Give the preparation type.
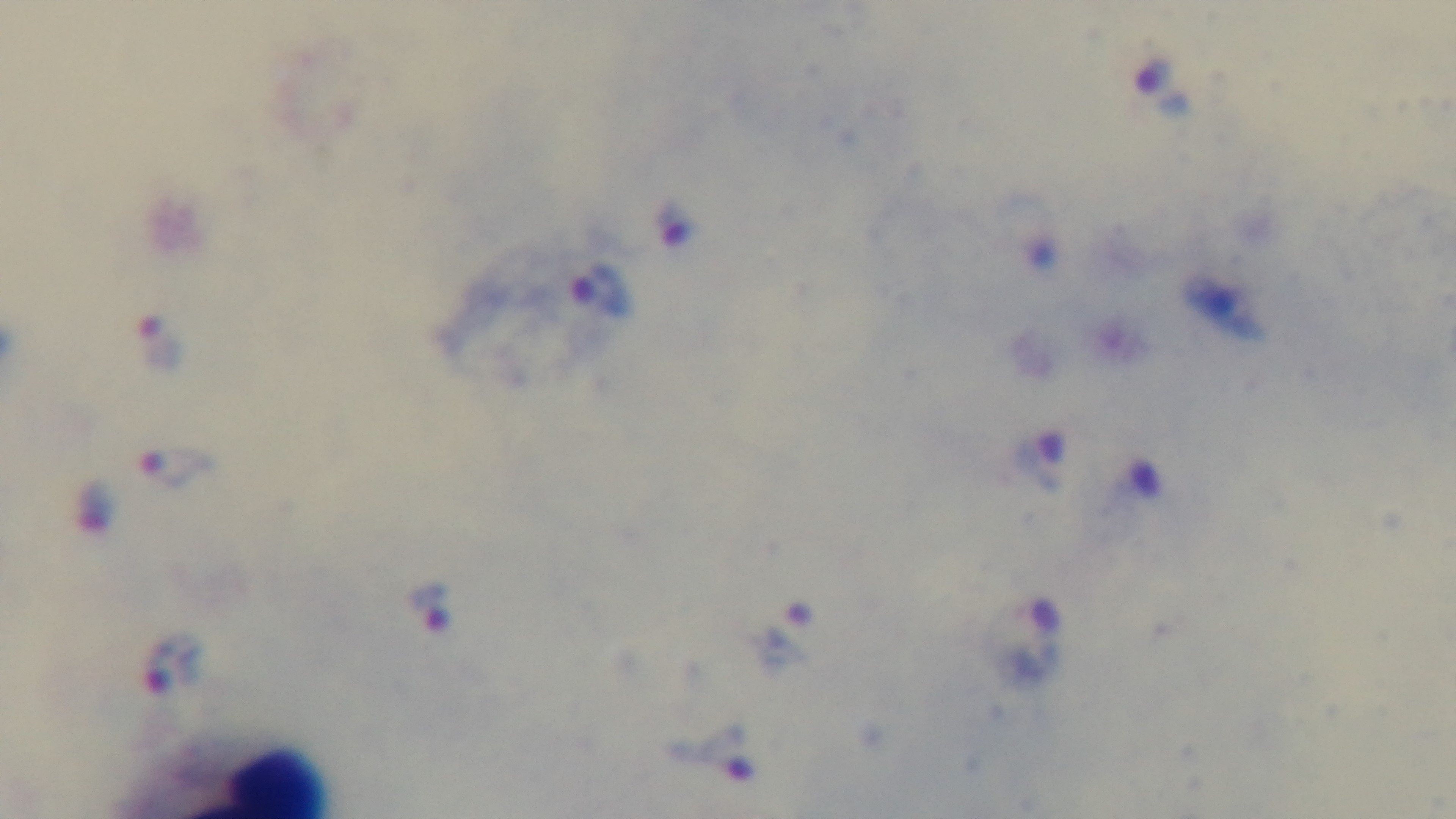
A thick smear.

Mounted 4K digital camera. Single field of view. Malaria status: infected. Giemsa-stained. 100x oil-immersion objective. Light microscopy.